Assess the morphology of the erythrocytes.
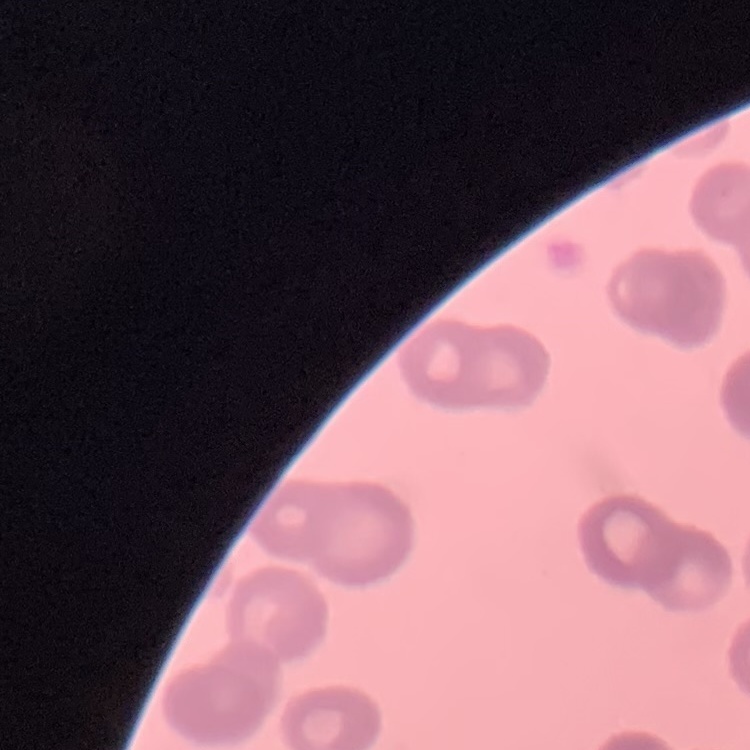

Rouleaux formation.

Summary:
  - Preparation: thin blood smear
  - Image type: one tile cut from a larger photomicrograph
  - Stain: Field's or Giemsa